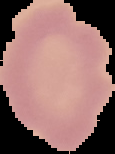

Summary:
  - Image type: cell region segmented out of the field of view; surrounding area masked to black
  - Malaria status: uninfected
  - Image size: 115×154 pixels
  - Preparation: thin blood film